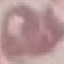

malaria status = uninfected
stain = Giemsa
capture = smartphone through the microscope eyepiece
image type = cell patch, automatically extracted from a larger field of view and resized to 64 × 64 pixels
preparation = thin blood smear